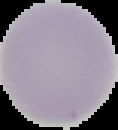
{
  "image_size": "118×130 pixels",
  "preparation": "thin blood smear",
  "image_type": "segmented cell region on a black background",
  "malaria_status": "uninfected"
}